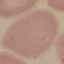

Malaria status: uninfected. Giemsa-stained preparation. Thin blood film. Acquired by smartphone through the microscope eyepiece. Automatically extracted cell patch, resized to 64 × 64 pixels.